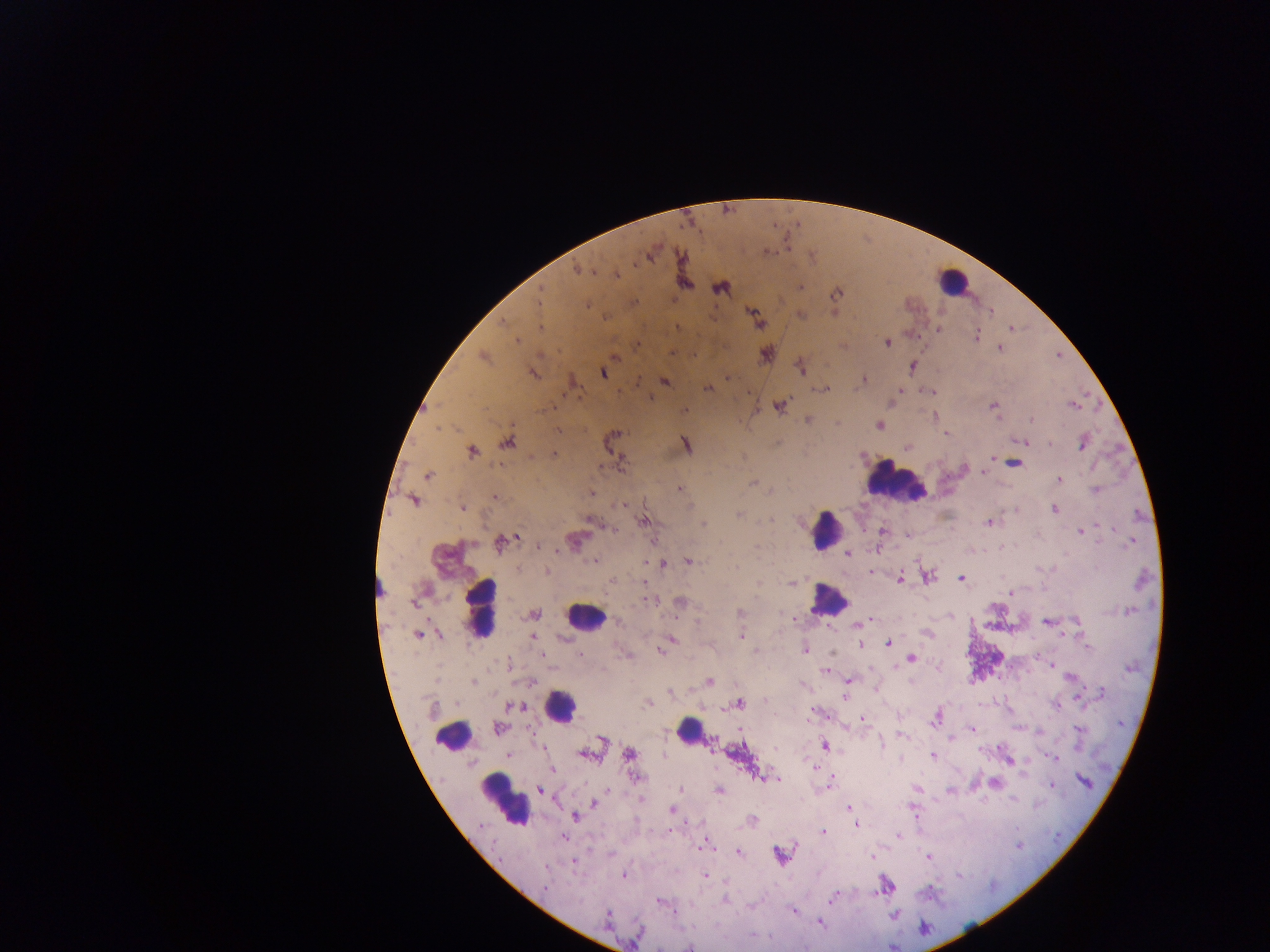

Approximate centers as (x, y) in pixels.
Summary:
  - Plasmodium parasite locations: (648, 257), (576, 269), (542, 293), (538, 304), (589, 305), (505, 320), (537, 324), (675, 326), (939, 330), (976, 336), (518, 341), (887, 344), (673, 351), (614, 356), (481, 357), (533, 373), (605, 375), (725, 376), (640, 380), (863, 380), (571, 381), (665, 381), (707, 388), (827, 388), (900, 394), (649, 396), (686, 407), (1067, 407), (1071, 407), (429, 409), (995, 409), (997, 414), (933, 415), (808, 420), (1030, 420), (837, 424), (879, 424), (438, 427), (559, 430), (947, 434), (507, 440), (1023, 442), (686, 444), (1051, 444), (1082, 447), (471, 451), (553, 453), (618, 458), (992, 458), (1016, 463), (964, 464), (983, 473), (427, 476), (1059, 480), (752, 481), (678, 487), (1094, 490), (590, 491), (494, 495), (414, 499), (621, 505), (463, 507), (1053, 510), (739, 514), (769, 519), (588, 521), (644, 521), (988, 522), (703, 523), (1101, 525), (612, 527), (882, 531), (1081, 531), (518, 536), (906, 536), (577, 539), (498, 541), (1129, 541), (469, 542), (538, 546), (561, 551), (848, 553), (593, 559), (645, 561), (688, 561), (659, 563), (547, 571), (899, 578), (928, 578), (961, 578), (790, 582), (645, 584), (379, 591), (1011, 593), (414, 600), (651, 601), (678, 601), (541, 611), (864, 621), (1075, 621), (1046, 623), (417, 634), (741, 637), (533, 638), (672, 638), (888, 643), (859, 646), (1088, 647), (804, 648), (661, 653), (832, 653), (580, 655), (542, 656), (911, 659), (1051, 666), (937, 667), (824, 670), (472, 680), (708, 680), (849, 680), (910, 680), (529, 681), (876, 689), (668, 693), (1102, 693), (845, 697), (649, 703), (741, 703), (509, 706), (523, 707), (862, 719), (937, 721), (497, 727), (739, 728), (1077, 728), (971, 729), (1039, 733), (902, 736), (602, 739), (951, 739), (881, 744), (825, 745), (541, 746), (710, 746), (626, 754), (510, 756), (583, 756), (664, 756), (932, 756), (900, 759), (1055, 760), (1008, 762), (811, 765), (553, 769), (1023, 775), (775, 779), (1086, 783), (828, 786), (1050, 786), (680, 789), (719, 789), (540, 790), (917, 790), (948, 790), (606, 791), (950, 792), (1012, 799), (641, 800), (592, 803), (848, 806), (671, 809), (576, 818), (857, 827), (823, 831), (897, 837), (564, 838), (701, 845), (1019, 845), (739, 853), (872, 854), (782, 856), (928, 859), (575, 863), (622, 875), (704, 876), (544, 889), (881, 892), (829, 901), (660, 902), (794, 910), (894, 915), (820, 923), (689, 946)
  - Leukocyte locations: (952, 283), (899, 479), (826, 531), (825, 600), (487, 608), (581, 618), (560, 704), (683, 729), (459, 738), (501, 802)
  - Capture: mobile-phone photograph through a microscope
  - Field of view: single
  - Country: Ghana
  - Preparation: thick blood film
  - Image size: 1270×952 pixels